Give the extent of all uninfected red blood cells.
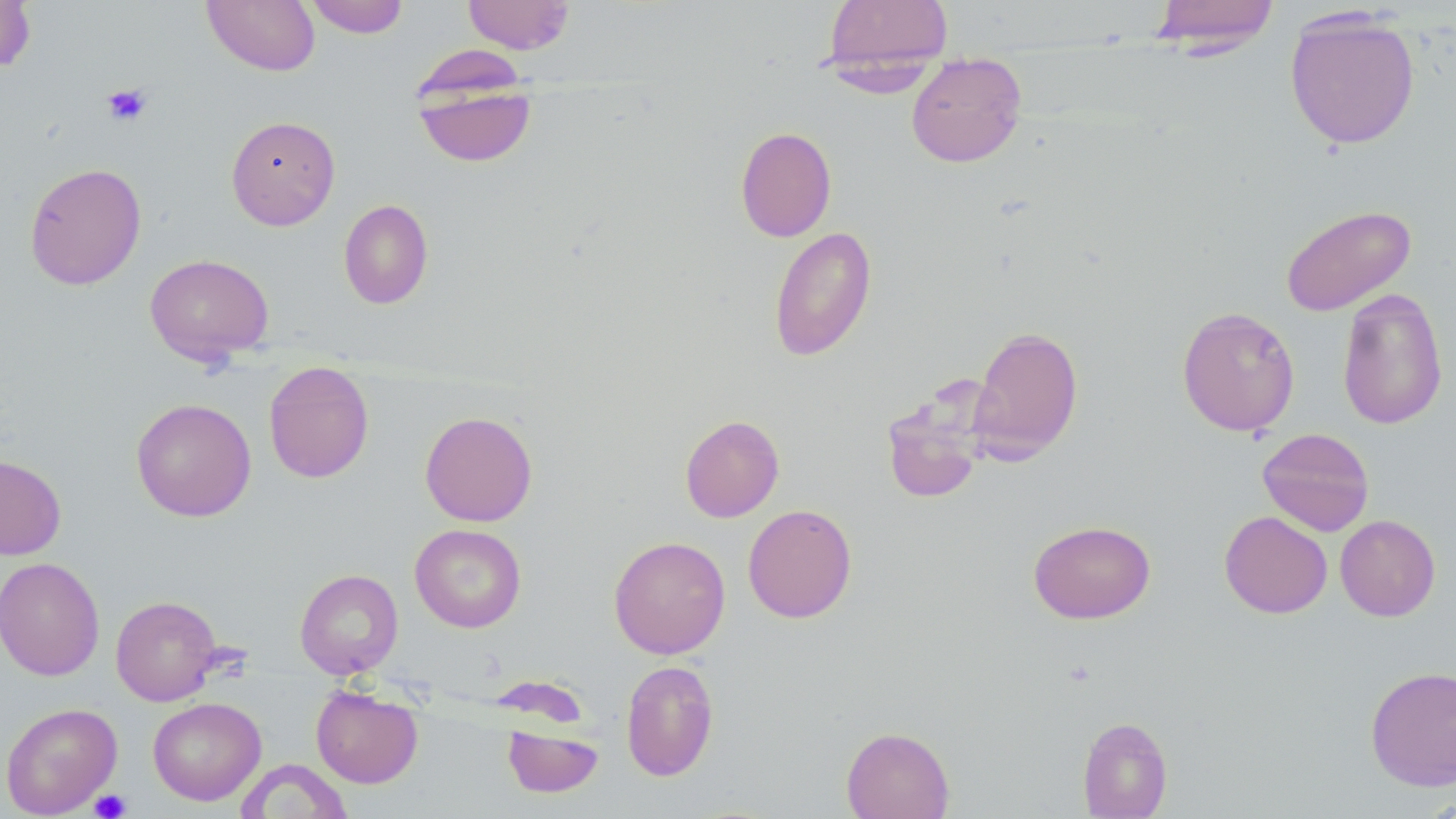
Approximate bounding boxes as (x1,y1)-(x2,y2) corner pairs in pixels.
Uninfected red blood cells: (0,0)-(35,72), (201,0)-(320,76), (304,0)-(410,38), (462,0)-(576,54), (820,0)-(954,83), (1148,0)-(1281,55), (1283,9)-(1421,150), (906,53)-(1027,168), (413,78)-(536,168), (226,115)-(341,230), (735,126)-(837,242), (24,162)-(147,290), (338,199)-(433,309), (1280,204)-(1416,316), (768,226)-(877,361), (144,254)-(274,365), (1336,287)-(1448,430), (1177,305)-(1300,437), (968,325)-(1084,463), (263,361)-(374,483), (881,386)-(991,505), (131,397)-(257,522), (419,410)-(538,526), (680,414)-(784,522), (1257,427)-(1375,536), (0,454)-(67,560), (742,504)-(857,623), (1219,511)-(1333,618), (1335,515)-(1440,621), (1028,519)-(1156,624), (410,523)-(527,633), (608,535)-(730,659), (0,556)-(104,681), (295,569)-(403,677), (110,595)-(223,706), (620,659)-(719,781), (1365,665)-(1456,791), (311,685)-(423,789), (148,696)-(266,805), (1,702)-(122,818), (1077,716)-(1172,818), (502,724)-(604,798), (840,726)-(955,819), (237,760)-(352,818).

slide-level diagnosis = negative for blood parasites
preparation = thin blood smear
platelet locations = approximate bounding boxes as (x1,y1)-(x2,y2) corner pairs in pixels: (101,83)-(153,127), (89,788)-(132,818)
magnification = 1000x
stain = May-Grünwald-Giemsa
modality = light microscopy
image size = 1456×819 pixels
field of view = single